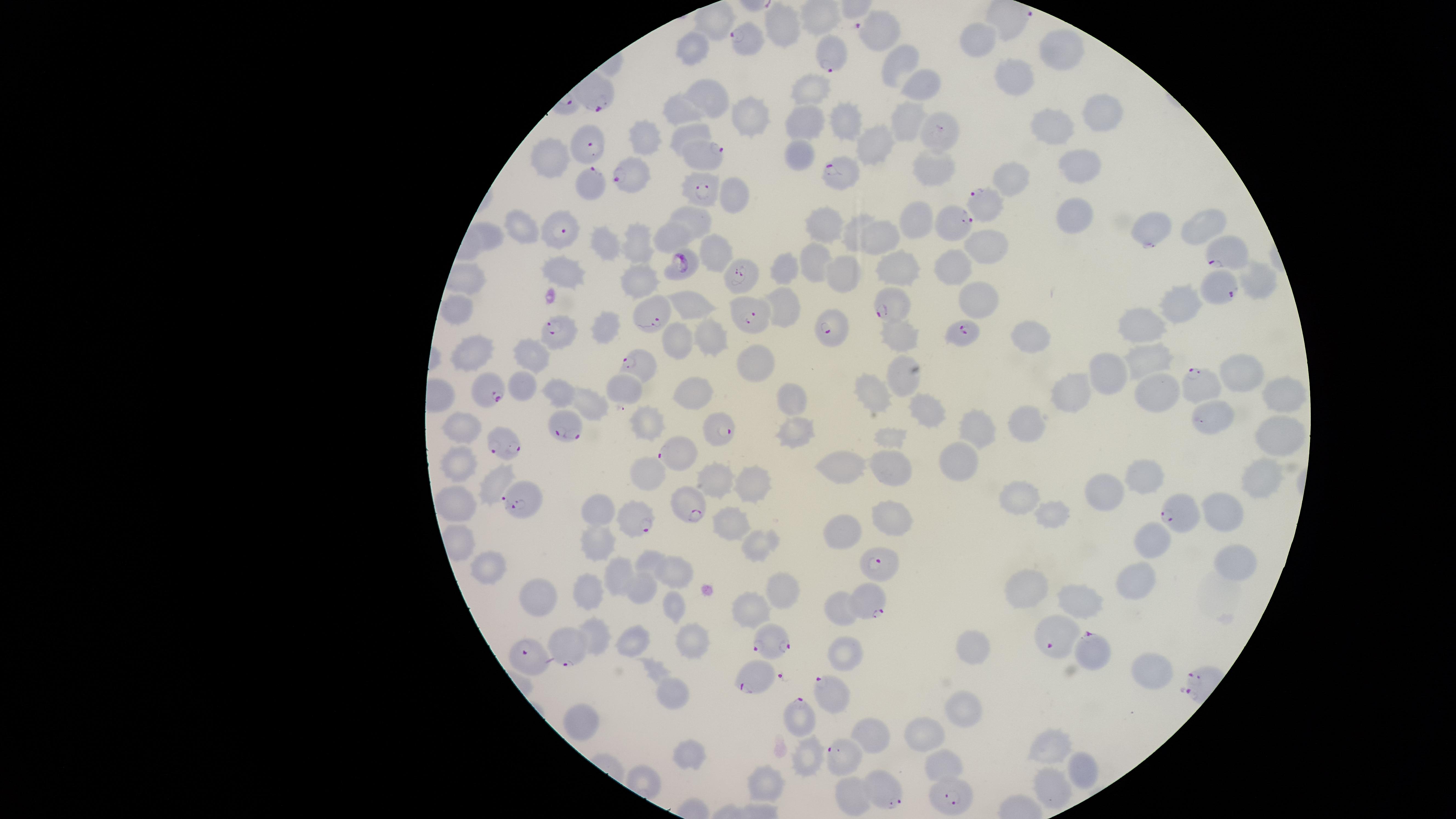
image size = 1456×819 pixels
stain = Giemsa
uninfected red blood cells = approximate marker points as (x, y) in pixels: (783, 30), (981, 41), (1057, 46), (695, 51), (903, 60), (1017, 78), (922, 85), (814, 86), (709, 95), (686, 106), (748, 112), (1091, 114), (805, 117), (844, 120), (902, 121), (1054, 128), (694, 131), (649, 136), (870, 143), (803, 151), (555, 155), (1080, 155), (931, 162), (1024, 176), (729, 196), (1072, 211), (698, 219), (919, 222), (821, 223), (1197, 223), (852, 229), (1144, 229), (523, 230), (668, 237), (638, 239), (884, 239), (603, 241), (991, 244), (716, 250), (812, 259), (892, 266), (566, 267), (958, 268), (785, 269), (843, 271), (1260, 280), (634, 282), (1187, 300), (980, 301), (693, 304), (785, 305), (453, 306), (1147, 325), (601, 327), (902, 334), (1032, 337), (713, 339), (681, 343), (479, 347), (527, 355), (1154, 358), (751, 359), (1109, 367), (1239, 369), (902, 374), (522, 386), (1158, 387), (1283, 387), (620, 389), (1075, 390), (553, 392), (702, 392), (792, 392), (873, 393), (591, 400), (926, 405), (1216, 409), (651, 417), (1029, 421), (974, 430), (1279, 430), (462, 431), (794, 432), (890, 438), (956, 457), (464, 462), (847, 463), (890, 463), (652, 470), (722, 474), (1150, 478), (498, 479), (1256, 480), (1107, 487), (756, 489), (1023, 499), (458, 503), (604, 508), (1222, 512), (890, 513), (1054, 513), (844, 527), (732, 528), (597, 531), (764, 539), (1158, 539), (649, 555), (1234, 560), (493, 566), (624, 567), (674, 570), (591, 583), (1136, 583), (643, 584), (782, 584), (1032, 587), (543, 595), (1080, 599), (676, 602), (752, 606), (843, 608), (597, 628), (635, 634), (696, 640), (974, 646), (847, 653), (1148, 671), (671, 692), (961, 714), (586, 719), (925, 730), (868, 731), (1054, 743), (691, 744), (811, 757), (942, 762), (1080, 765), (768, 780), (1049, 786), (855, 797)
parasitized red blood cells = approximate marker points as (x, y) in pixels: (883, 27), (744, 37), (829, 64), (587, 142), (700, 153), (844, 172), (634, 176), (588, 178), (703, 187), (987, 202), (952, 224), (563, 227), (1226, 252), (685, 266), (742, 277), (1220, 286), (888, 300), (651, 312), (748, 317), (558, 327), (826, 327), (961, 330), (637, 365), (1197, 379), (485, 391), (565, 426), (727, 427), (506, 440), (680, 455), (522, 499), (687, 508), (1184, 512), (631, 522), (879, 562), (873, 599), (1050, 635), (776, 640), (567, 647), (1085, 649), (529, 656), (757, 683), (835, 694), (796, 714), (843, 752), (889, 791), (946, 791)
presence = malaria parasites identified
capture = smartphone photograph through the microscope eyepiece
preparation = thin blood smear
field of view = single
species = Plasmodium falciparum
visible region = circular